State the blood parasite species.
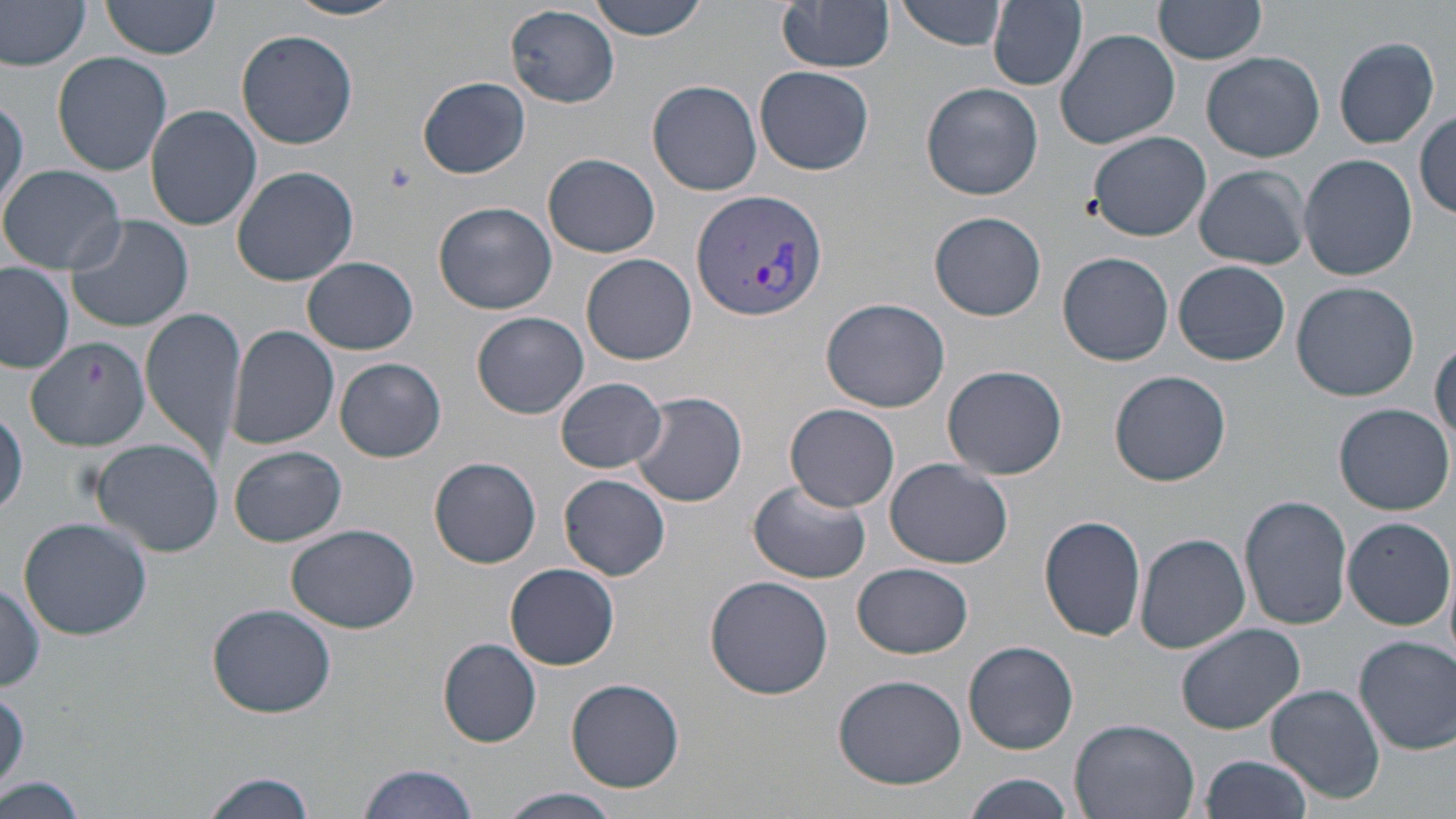
Plasmodium vivax.

stain: May-Grünwald-Giemsa
field_of_view: one of a larger specimen
plasmodium_vivax_infected_red_blood_cell_locations: 'approximate bounding boxes as named x1/y1/x2/y2 corners in pixels: (x1=689, y1=187, x2=828, y2=324)'
preparation: thin blood smear
image_size: 1456×819 pixels
magnification: 1000x
modality: optical microscopy
uninfected_red_blood_cell_locations: 'approximate bounding boxes as named x1/y1/x2/y2 corners in pixels: (x1=100, y1=0, x2=222, y2=58), (x1=285, y1=0, x2=408, y2=20), (x1=588, y1=0, x2=710, y2=39), (x1=900, y1=0, x2=1009, y2=51), (x1=775, y1=1, x2=896, y2=73), (x1=988, y1=1, x2=1087, y2=90), (x1=1153, y1=1, x2=1267, y2=67), (x1=1, y1=2, x2=89, y2=72), (x1=503, y1=4, x2=619, y2=110), (x1=236, y1=29, x2=359, y2=150), (x1=1055, y1=29, x2=1180, y2=150), (x1=1332, y1=37, x2=1440, y2=149), (x1=1202, y1=51, x2=1325, y2=163), (x1=52, y1=52, x2=172, y2=176), (x1=754, y1=65, x2=874, y2=175), (x1=418, y1=76, x2=531, y2=178), (x1=647, y1=80, x2=762, y2=196), (x1=922, y1=82, x2=1043, y2=202), (x1=0, y1=92, x2=27, y2=224), (x1=146, y1=103, x2=262, y2=231), (x1=1415, y1=112, x2=1455, y2=221), (x1=1085, y1=130, x2=1211, y2=242), (x1=544, y1=152, x2=660, y2=258), (x1=1299, y1=153, x2=1418, y2=280), (x1=1, y1=163, x2=125, y2=274), (x1=1193, y1=165, x2=1311, y2=269), (x1=230, y1=167, x2=359, y2=286), (x1=433, y1=201, x2=559, y2=315), (x1=928, y1=210, x2=1048, y2=322), (x1=65, y1=213, x2=194, y2=332), (x1=1058, y1=251, x2=1174, y2=366), (x1=582, y1=253, x2=698, y2=364), (x1=302, y1=257, x2=419, y2=355), (x1=1174, y1=260, x2=1290, y2=366), (x1=0, y1=262, x2=74, y2=374), (x1=1291, y1=280, x2=1420, y2=401), (x1=821, y1=297, x2=951, y2=412), (x1=141, y1=306, x2=247, y2=466), (x1=473, y1=312, x2=590, y2=420), (x1=226, y1=324, x2=340, y2=450), (x1=23, y1=335, x2=150, y2=447), (x1=1431, y1=342, x2=1455, y2=446), (x1=334, y1=358, x2=447, y2=463), (x1=942, y1=364, x2=1068, y2=480), (x1=1109, y1=370, x2=1232, y2=487), (x1=556, y1=377, x2=668, y2=473), (x1=629, y1=390, x2=748, y2=507), (x1=1334, y1=403, x2=1454, y2=515), (x1=786, y1=404, x2=901, y2=511), (x1=1, y1=409, x2=27, y2=521), (x1=89, y1=439, x2=227, y2=557), (x1=228, y1=444, x2=347, y2=548), (x1=428, y1=456, x2=541, y2=569), (x1=884, y1=458, x2=1013, y2=570), (x1=560, y1=473, x2=670, y2=581), (x1=746, y1=476, x2=873, y2=583), (x1=1240, y1=496, x2=1353, y2=629), (x1=1039, y1=514, x2=1148, y2=643), (x1=1342, y1=516, x2=1453, y2=629), (x1=18, y1=517, x2=152, y2=642), (x1=287, y1=524, x2=422, y2=634), (x1=1135, y1=532, x2=1250, y2=654), (x1=852, y1=562, x2=973, y2=659), (x1=506, y1=563, x2=620, y2=669), (x1=705, y1=575, x2=834, y2=700), (x1=0, y1=578, x2=47, y2=694), (x1=207, y1=604, x2=337, y2=717), (x1=1175, y1=622, x2=1305, y2=734), (x1=1354, y1=635, x2=1456, y2=754), (x1=437, y1=638, x2=543, y2=748), (x1=962, y1=641, x2=1078, y2=755), (x1=833, y1=673, x2=967, y2=789), (x1=564, y1=678, x2=685, y2=792), (x1=0, y1=684, x2=29, y2=797), (x1=1267, y1=686, x2=1385, y2=802), (x1=1069, y1=719, x2=1200, y2=819), (x1=1198, y1=753, x2=1313, y2=819), (x1=358, y1=763, x2=477, y2=819), (x1=196, y1=771, x2=319, y2=818), (x1=963, y1=772, x2=1075, y2=819), (x1=0, y1=776, x2=90, y2=819), (x1=495, y1=787, x2=624, y2=818)'
platelet_locations: 'approximate bounding boxes as named x1/y1/x2/y2 corners in pixels: (x1=378, y1=158, x2=418, y2=198)'